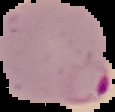 Image is 115×112 pixels. Cell region segmented out of the field of view; the surrounding area is masked to black. Result: malaria parasites identified. From a thin blood smear.